Assess this cell for malaria.
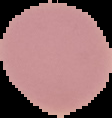
Uninfected.

{
  "preparation": "thin blood film",
  "image_type": "segmented cell region on a black background",
  "image_size": "112×118 pixels"
}